Identify the parasite.
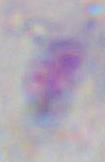

This is Toxoplasma gondii.

Summary:
  - Magnification: 1000x
  - Modality: photomicrograph